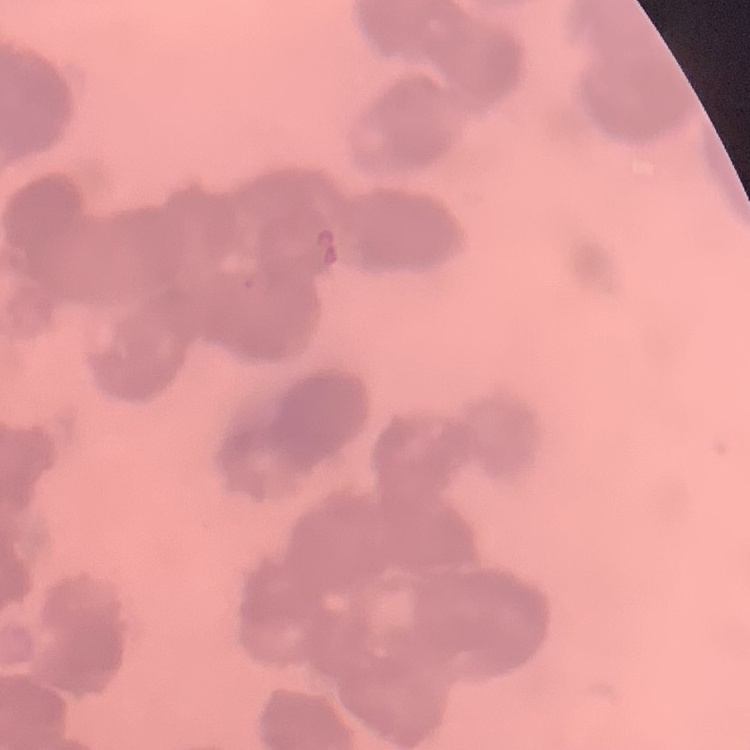

The erythrocytes show rouleaux formation. One tile cut from a larger photomicrograph. Field's or Giemsa stain. Thin peripheral smear.